Report the malaria status of this cell.
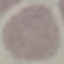

Uninfected.

Summary:
  - Capture: smartphone camera at the microscope eyepiece
  - Stain: Giemsa
  - Preparation: thin blood smear
  - Image type: automatically extracted cell patch, resized to 64 × 64 pixels